Assess the morphology of the red blood cells.
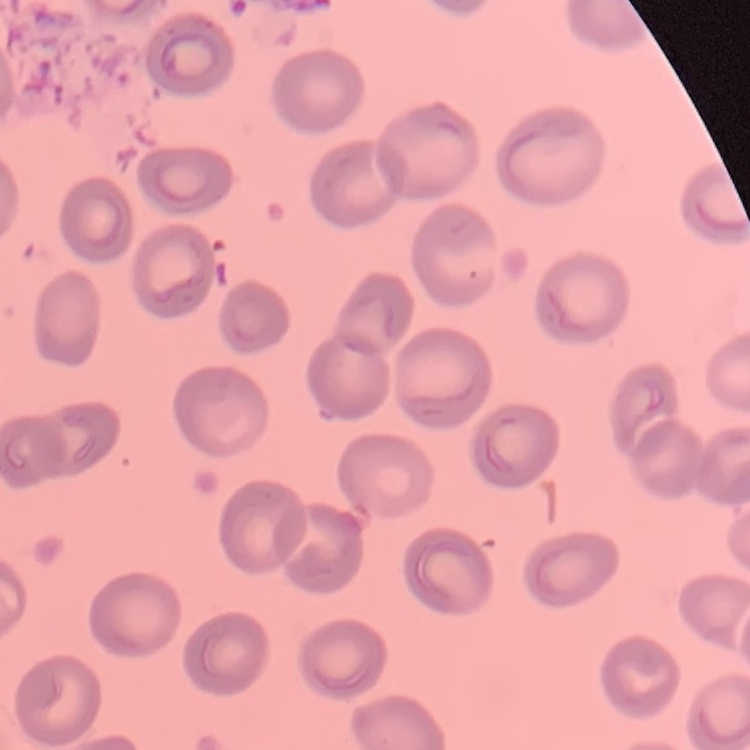

They show no rouleaux formation.

One tile cut from a larger photomicrograph. Thin peripheral smear. Stained with either Field's or Giemsa.